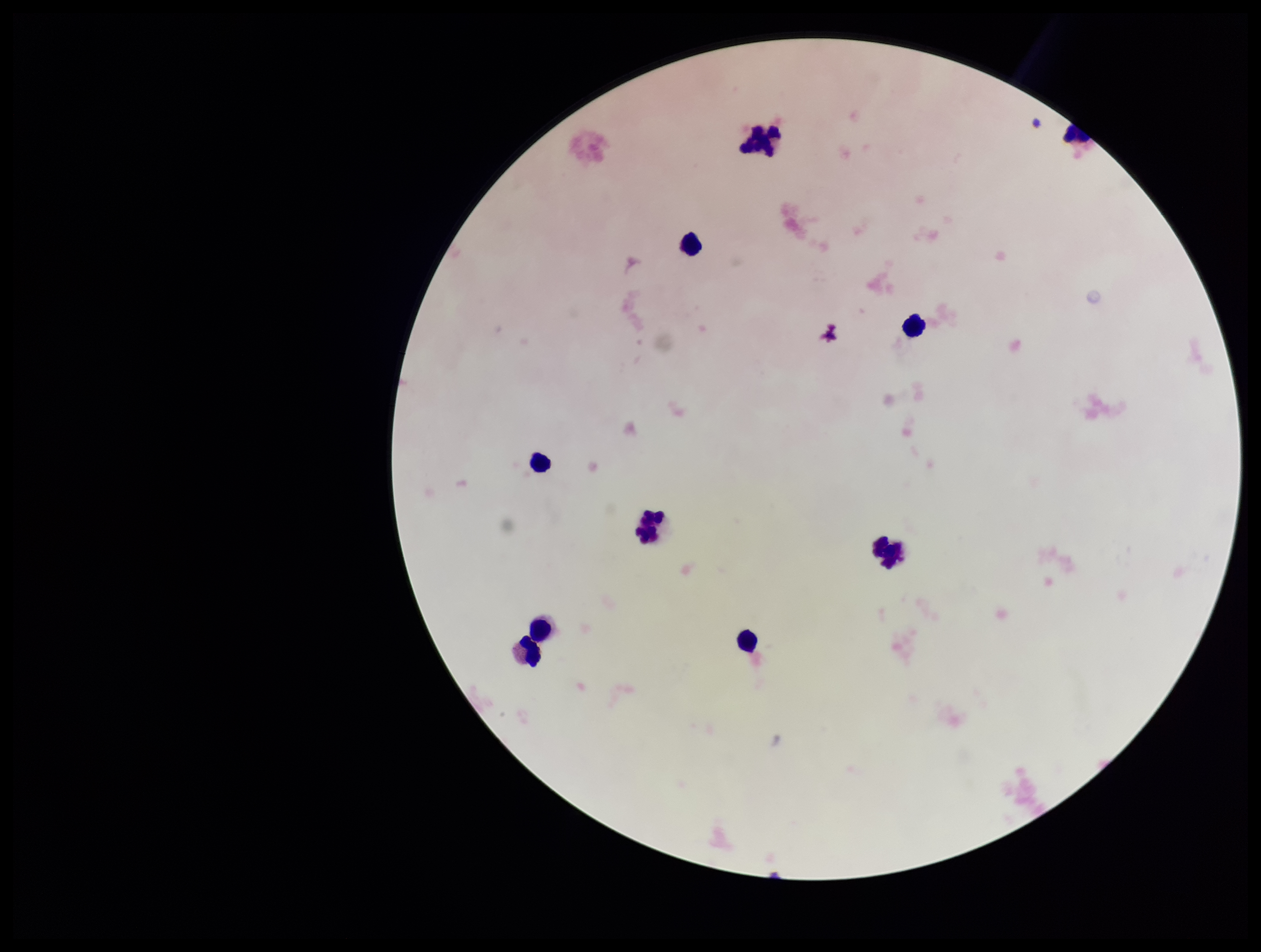

parasite count = 0
Plasmodium parasites = none identified
field of view = one from this slide
patient malaria status = negative
leukocyte count = 10
preparation = thick smear
image size = 1261×952 pixels
stain = Giemsa
capture = smartphone photograph through the microscope eyepiece